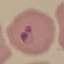

malaria status = parasitized
image type = cell patch, automatically extracted from a larger field of view and resized to 64 × 64 pixels
preparation = thin smear
capture = smartphone camera at the microscope eyepiece
stain = Giemsa